Report the malaria status of this cell.
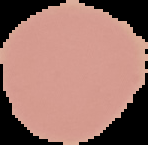

It is uninfected.

image_size: 148×145 pixels
image_type: segmented cell region with the area outside set to black
preparation: thin blood smear